State the preparation type.
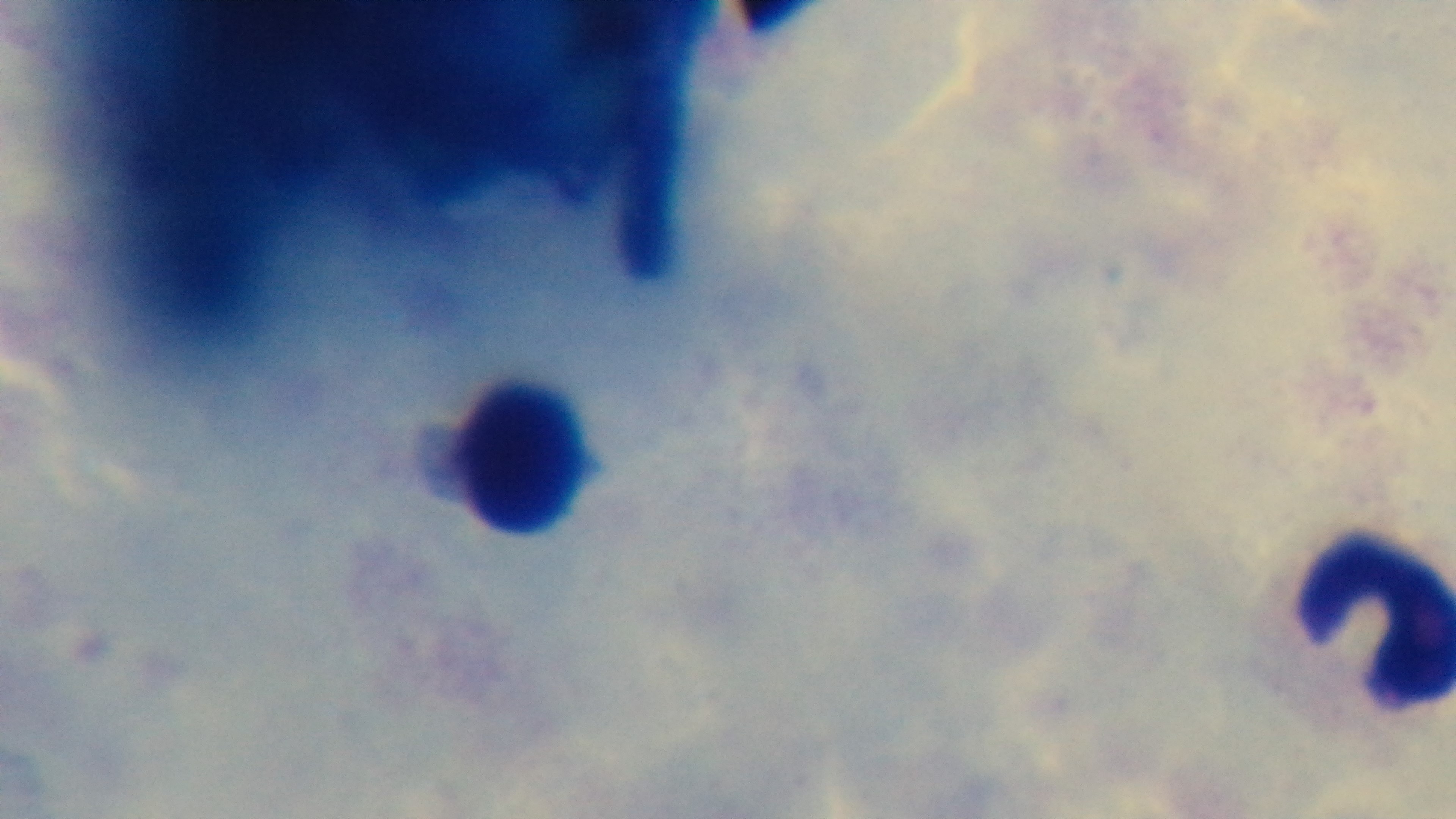
A thick smear.

Captured with a mounted 4K digital camera. Photomicrograph. Malaria status: negative. 100x oil-immersion objective. Single field of view. Giemsa-stained.